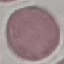
Summary:
  - Result: no malaria parasites detected
  - Capture: smartphone camera at the microscope eyepiece
  - Preparation: thin blood film
  - Stain: Giemsa
  - Image type: cell patch, automatically extracted from a larger field of view and resized to 64 × 64 pixels